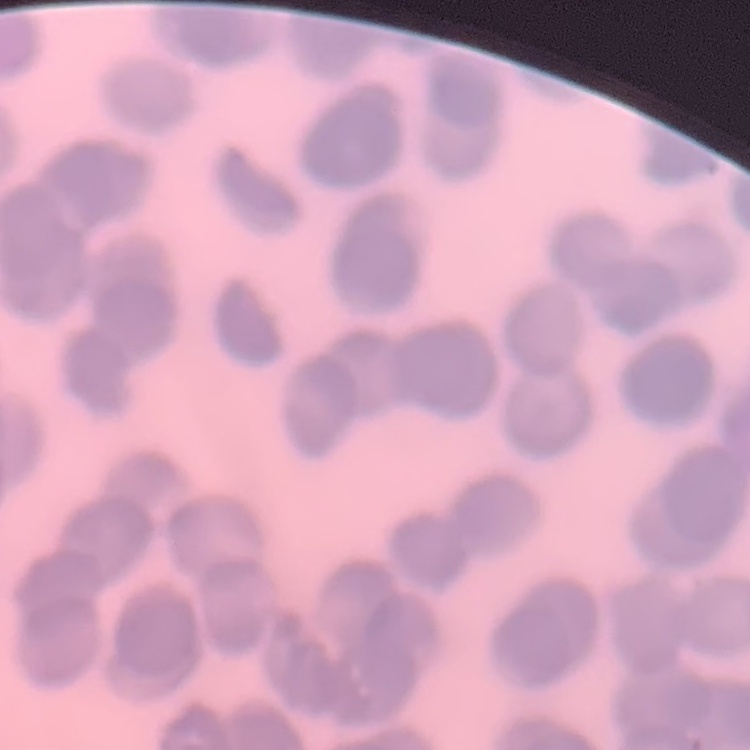

red blood cell morphology = rouleaux formation
stain = Field's or Giemsa
image type = square crop of a larger photomicrograph
preparation = thin peripheral smear